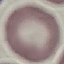

malaria status = uninfected
stain = Giemsa
preparation = thin blood film
image type = automatically extracted cell patch, resized to 64 × 64 pixels
capture = smartphone through the microscope eyepiece